Assess for malaria.
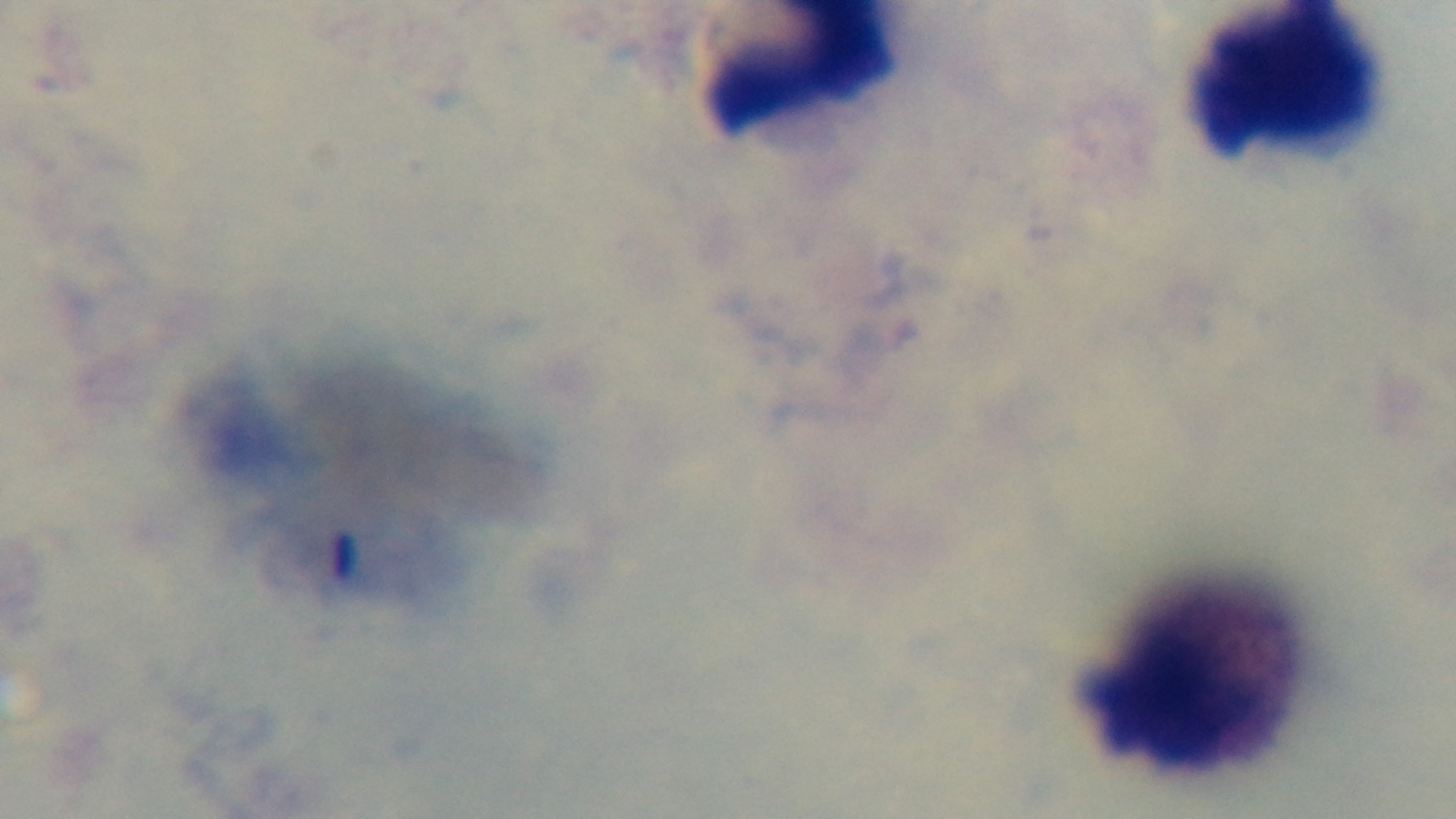
It is uninfected.

Preparation: thick smear. 100x oil-immersion objective. Captured with a mounted 4K digital camera. Light microscopy. Giemsa-stained. One field from the slide.